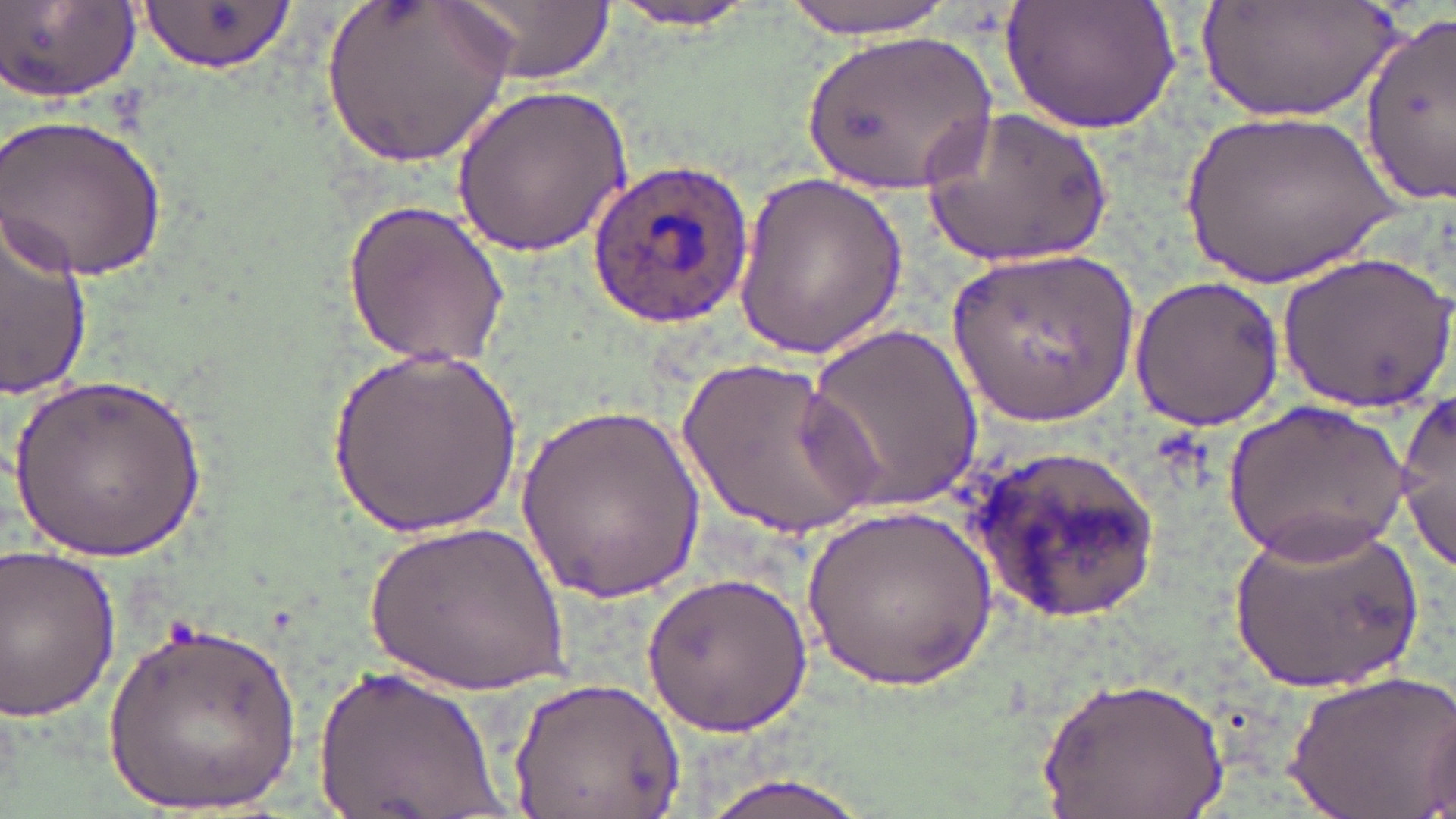
slide_level_diagnosis: Plasmodium ovale
preparation: thin blood film
magnification: 1000x
uninfected_red_blood_cell_locations: 'approximate bounding boxes as [x1, y1, x2, y2] in pixels: [321, 0, 516, 169], [447, 0, 612, 85], [602, 0, 767, 31], [771, 0, 964, 39], [1004, 0, 1182, 136], [1193, 0, 1400, 122], [4, 1, 143, 108], [140, 2, 294, 77], [1356, 12, 1456, 204], [802, 30, 996, 196], [447, 83, 632, 262], [921, 106, 1110, 269], [1176, 108, 1404, 295], [1, 111, 169, 284], [732, 172, 907, 359], [0, 201, 90, 402], [343, 201, 513, 369], [951, 248, 1142, 421], [1282, 250, 1452, 410], [1128, 275, 1286, 430], [803, 322, 982, 517], [329, 340, 522, 541], [672, 348, 885, 546], [10, 369, 206, 565], [1395, 396, 1455, 570], [1225, 397, 1408, 562], [518, 399, 703, 606], [961, 441, 1166, 625], [803, 504, 996, 693], [1230, 516, 1424, 700], [371, 517, 570, 690], [0, 539, 124, 727], [640, 570, 818, 737], [104, 616, 300, 819], [313, 661, 508, 819], [1281, 672, 1455, 816], [1041, 673, 1227, 819], [508, 680, 686, 818], [691, 770, 884, 819]'
modality: light microscopy
field_of_view: one of a larger specimen
plasmodium_ovale_infected_red_blood_cell_locations: 'approximate bounding boxes as [x1, y1, x2, y2] in pixels: [586, 159, 752, 331]'
image_size: 1456×819 pixels
stain: May-Grünwald-Giemsa